Name the blood parasite species.
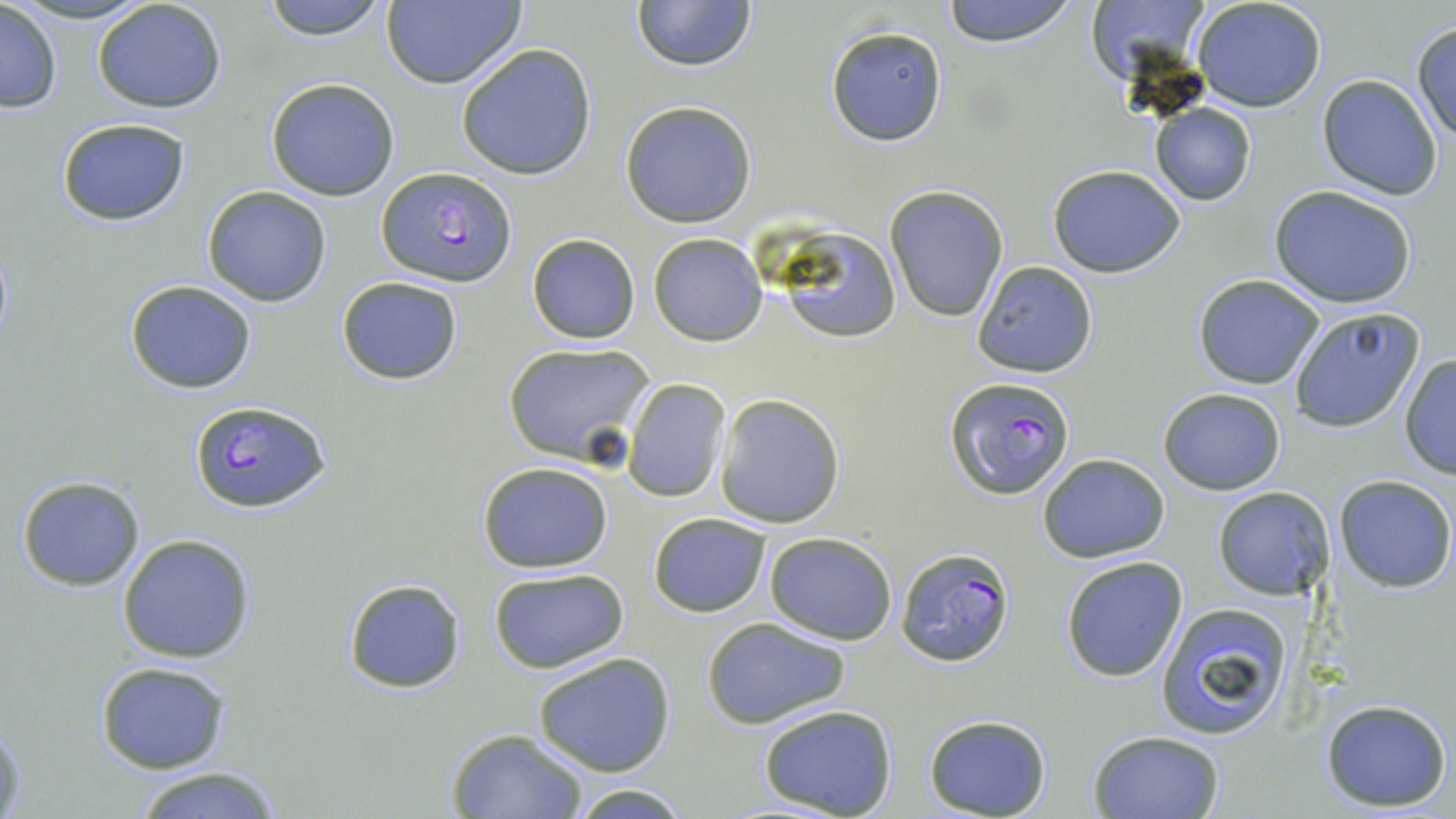

Plasmodium falciparum.

Approximate bounding boxes as [x1, y1, x2, y2] in pixels. Plasmodium falciparum-infected red blood cell locations: [377, 166, 515, 288], [947, 377, 1074, 499], [189, 399, 329, 513], [894, 546, 1016, 667]. Uninfected red blood cell locations: [259, 0, 392, 41], [940, 0, 1080, 46], [1083, 0, 1219, 88], [91, 1, 228, 115], [631, 1, 759, 72], [1191, 1, 1328, 112], [0, 2, 62, 114], [380, 2, 526, 89], [1411, 21, 1455, 146], [826, 25, 949, 147], [455, 42, 598, 180], [1317, 75, 1443, 198], [265, 78, 400, 202], [620, 99, 758, 228], [1148, 103, 1257, 206], [55, 119, 190, 225], [1047, 165, 1185, 277], [884, 185, 1009, 323], [1268, 186, 1416, 309], [201, 187, 332, 305], [775, 228, 902, 344], [648, 233, 768, 345], [527, 234, 639, 343], [973, 261, 1098, 378], [1192, 276, 1325, 390], [336, 277, 463, 385], [122, 279, 259, 394], [1287, 308, 1427, 433], [502, 341, 656, 466], [1399, 355, 1456, 478], [622, 378, 730, 502], [1158, 388, 1286, 494], [714, 394, 845, 528], [1037, 454, 1169, 563], [477, 460, 615, 572], [15, 476, 145, 590], [1333, 476, 1455, 591], [1212, 487, 1334, 601], [648, 513, 771, 617], [116, 532, 259, 664], [763, 532, 897, 643], [1060, 556, 1188, 682], [489, 568, 628, 675], [340, 577, 468, 696], [1156, 601, 1295, 740], [702, 618, 850, 730], [532, 652, 677, 776], [95, 661, 231, 774], [1319, 697, 1451, 813], [755, 705, 899, 818], [0, 712, 25, 818], [923, 714, 1053, 819], [446, 728, 589, 817], [1086, 729, 1225, 818], [125, 765, 288, 819], [567, 784, 692, 817]. Optical microscopy. One field of a larger specimen. May-Grünwald-Giemsa stain. Captured at 1000x magnification. Image is 1456×819 pixels. Thin blood smear.